Assess this cell for malaria.
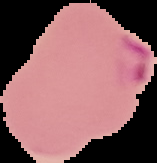
Parasitized.

Summary:
  - Image type: segmented cell region with the area outside set to black
  - Image size: 157×163 pixels
  - Preparation: thin blood film